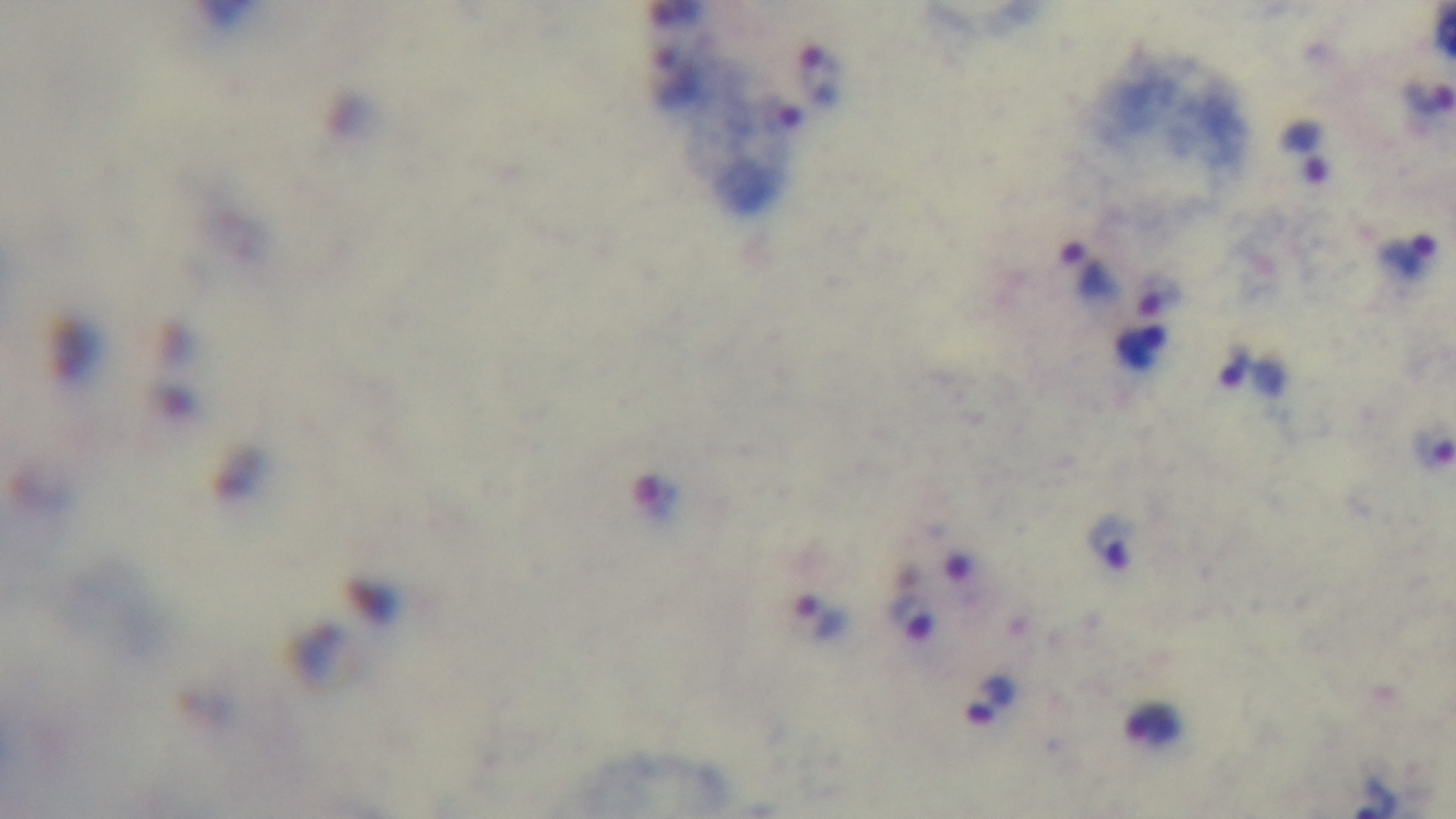
Summary:
  - Malaria status: positive
  - Modality: light microscopy
  - Field of view: one from the slide
  - Preparation: thick blood film
  - Stain: Giemsa
  - Objective: 100x oil immersion
  - Capture: mounted 4K digital camera